Assess the morphology of the erythrocytes.
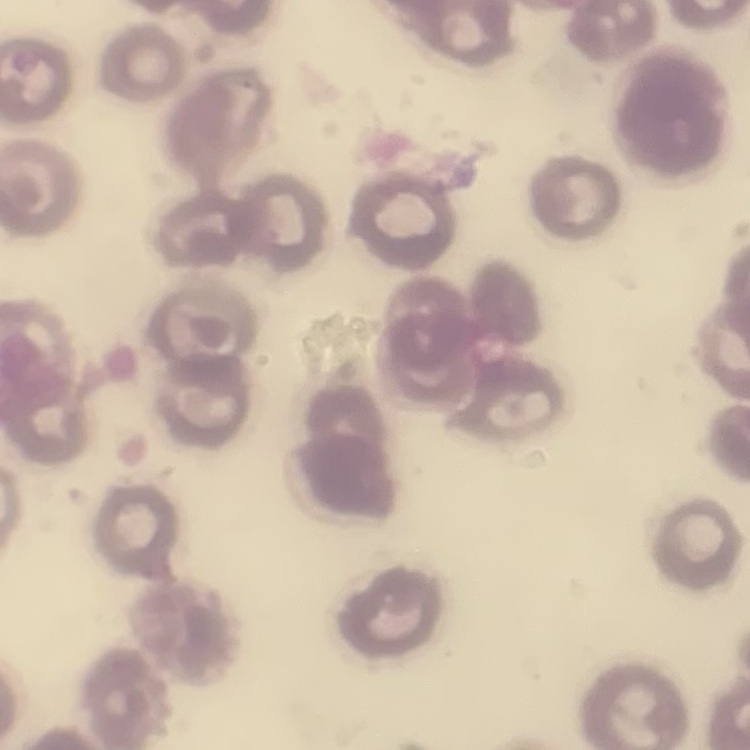

No rouleaux formation.

image_type: square crop of a larger photomicrograph
preparation: thin peripheral smear
stain: Field's or Giemsa